Assess this cell for malaria.
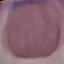

It is uninfected.

{
  "preparation": "thin blood film",
  "capture": "smartphone through the microscope eyepiece",
  "stain": "Giemsa",
  "image_type": "cell patch, automatically extracted from a larger field of view and resized to 64 × 64 pixels"
}